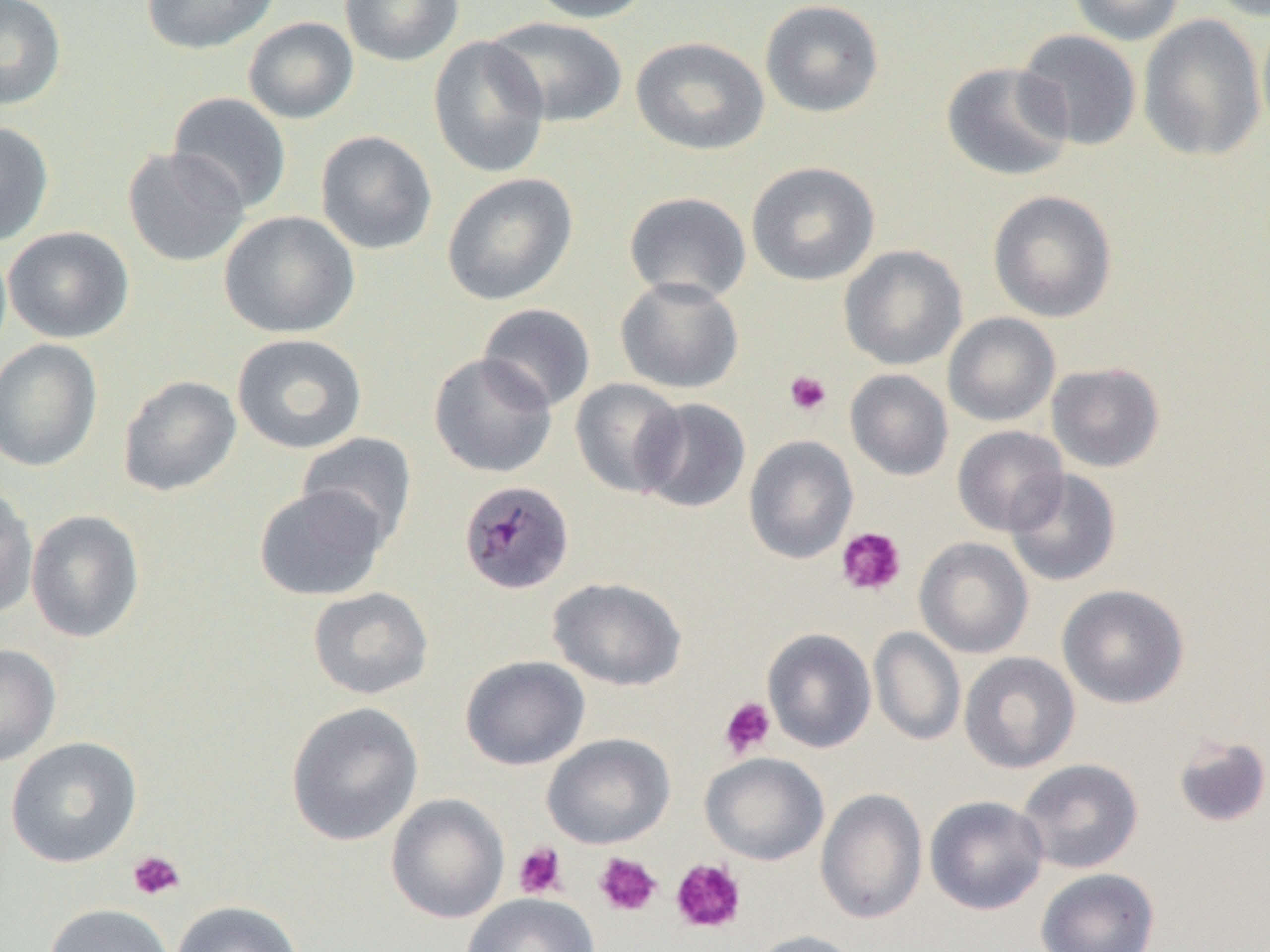 Approximate bounding boxes as (x1, y1, x2, y2) in pixels. Plasmodium malariae-infected red blood cell locations: (459, 479, 575, 595). Platelet locations: (785, 370, 832, 416), (836, 527, 907, 597), (719, 696, 776, 759), (513, 843, 567, 900), (127, 850, 185, 901), (594, 853, 662, 917), (670, 858, 747, 934). Uninfected red blood cell locations: (0, 0, 66, 110), (141, 0, 280, 55), (340, 0, 464, 66), (526, 0, 656, 24), (759, 0, 885, 118), (1068, 0, 1185, 46), (1207, 0, 1270, 21), (1138, 14, 1266, 162), (1257, 15, 1270, 140), (484, 16, 628, 128), (243, 17, 359, 124), (1015, 29, 1142, 151), (428, 36, 551, 179), (631, 36, 770, 155), (941, 61, 1075, 181), (167, 92, 292, 213), (0, 121, 54, 247), (315, 130, 438, 255), (122, 146, 250, 268), (746, 161, 880, 286), (442, 173, 578, 305), (987, 190, 1118, 323), (623, 191, 752, 304), (219, 210, 361, 339), (3, 226, 134, 344), (839, 244, 967, 370), (614, 276, 744, 394), (477, 303, 597, 412), (942, 312, 1060, 427), (231, 333, 368, 455), (0, 339, 103, 473), (428, 352, 557, 478), (1046, 362, 1165, 473), (846, 369, 953, 480), (117, 375, 242, 497), (570, 378, 687, 497), (635, 397, 751, 513), (952, 425, 1068, 536), (296, 432, 417, 545), (744, 435, 858, 564), (1004, 468, 1122, 587), (0, 483, 38, 619), (253, 485, 389, 601), (26, 509, 145, 643), (914, 537, 1033, 658), (547, 577, 687, 691), (1057, 584, 1190, 709), (308, 587, 434, 700), (869, 627, 966, 746), (763, 628, 877, 753), (0, 643, 61, 767), (959, 651, 1080, 774), (460, 654, 590, 771), (286, 701, 424, 846), (542, 733, 675, 849), (1172, 733, 1270, 829), (5, 736, 142, 868), (700, 752, 829, 865), (1016, 758, 1143, 874), (815, 788, 928, 925), (385, 793, 509, 923), (924, 795, 1049, 915), (1036, 868, 1160, 952), (461, 892, 600, 952), (170, 901, 304, 952), (44, 903, 174, 952), (745, 930, 866, 952). Slide-level diagnosis: Plasmodium malariae. One field of a larger specimen. Optical microscopy. 1000x magnification. Thin blood film. Image is 1270×952 pixels.